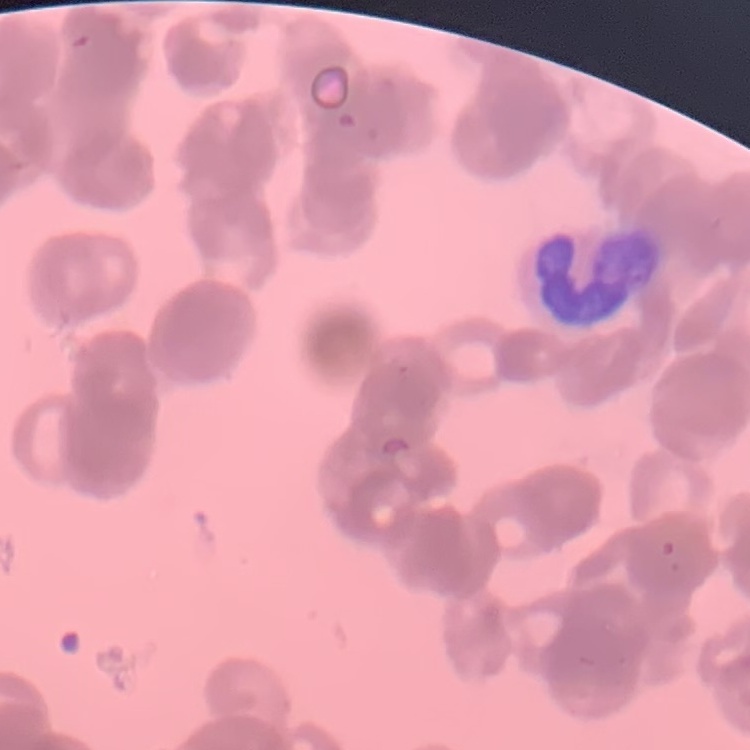 The erythrocytes show rouleaux formation. Field's or Giemsa stain. Thin blood smear. One tile cut from a larger photomicrograph.